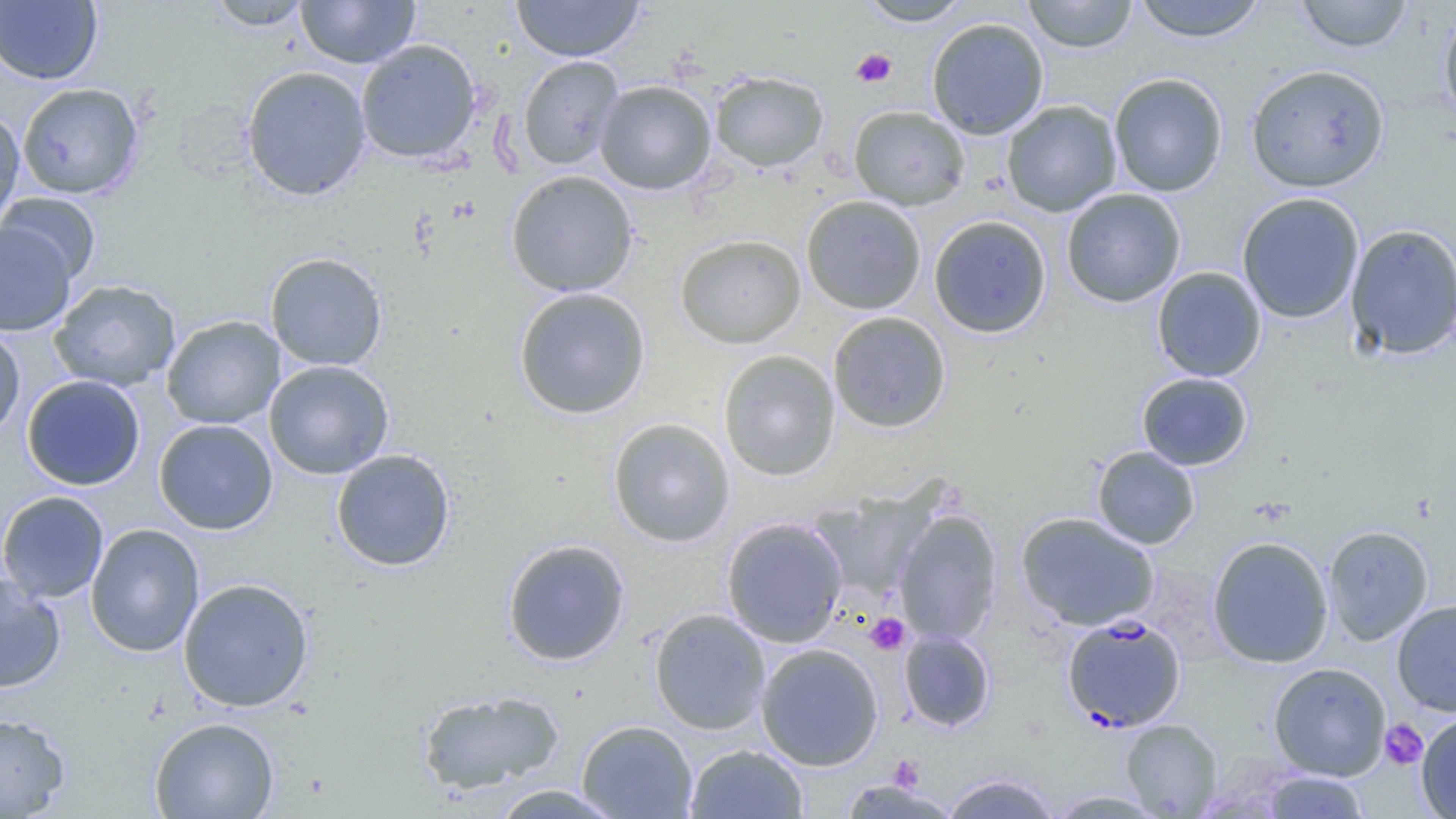

Approximate bounding boxes as (x1, y1, x2, y2) in pixels. Uninfected red blood cell locations: (207, 0, 312, 31), (296, 0, 420, 68), (512, 0, 644, 62), (857, 0, 974, 26), (1022, 0, 1138, 53), (1131, 0, 1269, 42), (1294, 0, 1414, 52), (0, 1, 103, 85), (1438, 6, 1456, 130), (926, 17, 1050, 140), (355, 39, 482, 163), (517, 56, 623, 170), (1245, 63, 1391, 193), (241, 65, 372, 201), (709, 70, 828, 173), (1109, 73, 1228, 197), (595, 80, 716, 194), (16, 82, 145, 200), (1002, 100, 1122, 217), (848, 105, 970, 211), (0, 108, 25, 231), (506, 170, 638, 296), (1061, 188, 1187, 307), (0, 192, 101, 286), (1236, 192, 1365, 324), (801, 195, 927, 315), (929, 215, 1052, 338), (0, 222, 77, 336), (1344, 223, 1456, 360), (675, 233, 807, 349), (265, 252, 388, 371), (1151, 267, 1266, 382), (49, 279, 181, 392), (513, 287, 651, 419), (827, 311, 951, 433), (161, 315, 285, 429), (0, 324, 26, 442), (718, 349, 840, 481), (264, 360, 394, 480), (1137, 372, 1253, 470), (21, 375, 146, 491), (607, 417, 736, 547), (153, 419, 278, 535), (1092, 446, 1200, 549), (330, 449, 456, 572), (0, 490, 109, 603), (811, 490, 937, 603), (893, 509, 1003, 645), (1016, 511, 1160, 631), (721, 516, 848, 648), (85, 523, 205, 657), (1322, 524, 1434, 645), (1207, 535, 1334, 669), (501, 538, 631, 667), (0, 573, 66, 693), (177, 577, 314, 712), (1392, 599, 1456, 716), (648, 608, 771, 734), (898, 629, 996, 732), (755, 643, 884, 771), (1268, 662, 1391, 780), (416, 688, 565, 795), (0, 712, 70, 818), (1416, 713, 1456, 818), (149, 716, 280, 819), (577, 719, 698, 819), (1121, 719, 1222, 818), (685, 744, 809, 818), (939, 771, 1061, 819), (1261, 771, 1369, 818), (837, 778, 961, 819), (489, 784, 626, 819), (1045, 790, 1170, 818). Plasmodium falciparum-infected red blood cell locations: (1062, 614, 1186, 732). Platelet locations: (851, 48, 897, 87), (865, 613, 910, 655), (1380, 720, 1427, 770). Slide-level diagnosis: Plasmodium falciparum. Thin blood smear. Image is 1456×819 pixels. Optical microscopy. Single field of view. 1000x magnification.